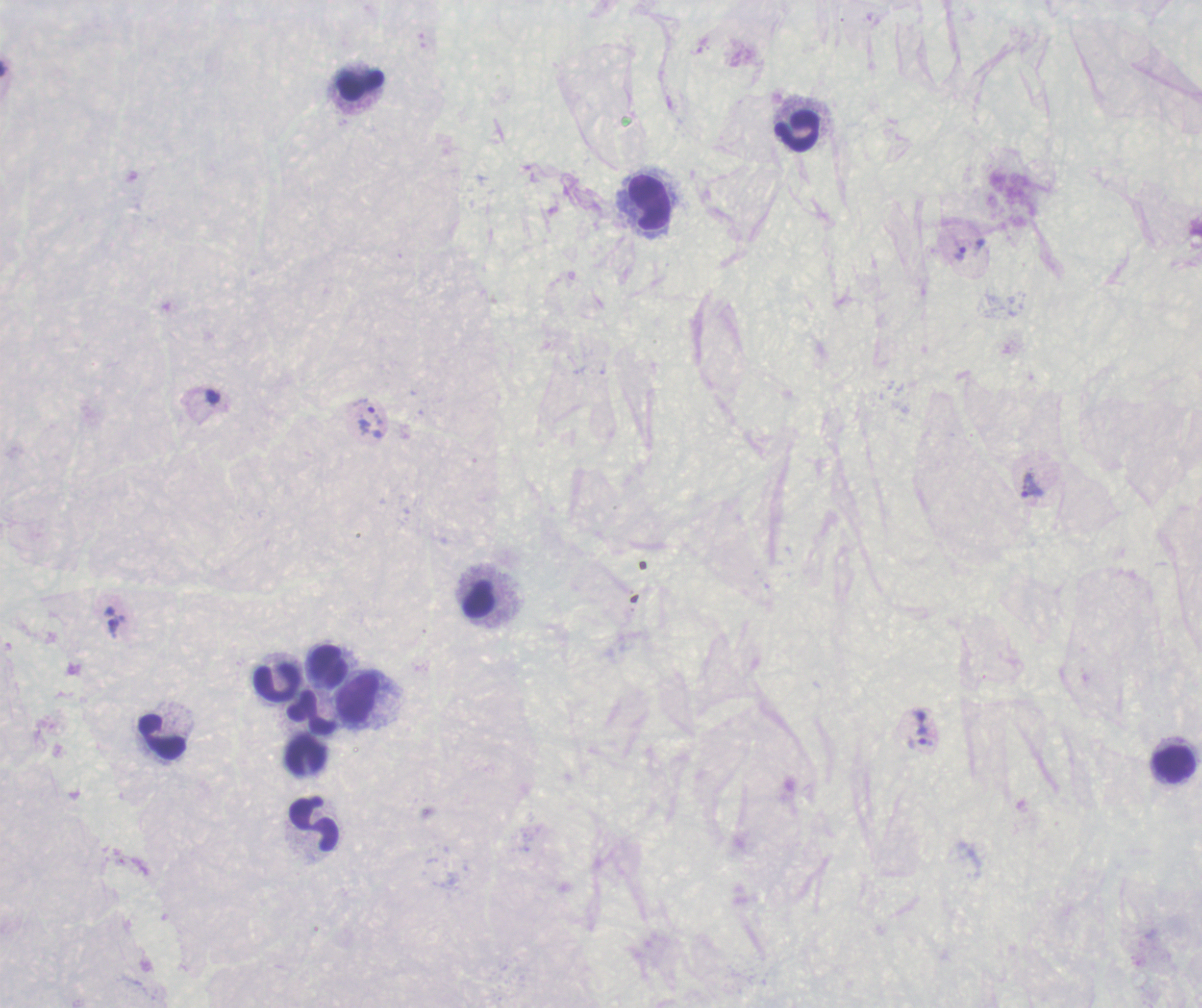
Approximate centers as {x, y} in pixels.
Summary:
  - Leukocyte locations: {360, 85}, {797, 131}, {649, 203}, {327, 666}, {279, 681}, {357, 700}, {312, 711}, {163, 737}, {306, 756}, {1174, 762}, {314, 826}
  - Trophozoite locations: {961, 255}, {213, 397}, {375, 416}, {1032, 486}, {113, 629}, {923, 736}
  - Coloration quality: bad
  - Magnification: 100x
  - Result: Plasmodium parasites detected
  - Stain: Romanowsky
  - Context: previously used in a real diagnosis
  - Field of view: one from this slide
  - Preparation: thick blood smear
  - Image size: 1202×1008 pixels
  - Background quality: poor